Report the malaria status of this cell.
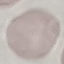

Uninfected.

stain: Giemsa
preparation: thin smear
capture: smartphone camera at the microscope eyepiece
image_type: automatically extracted cell patch, resized to 64 × 64 pixels